Identify the blood parasite species.
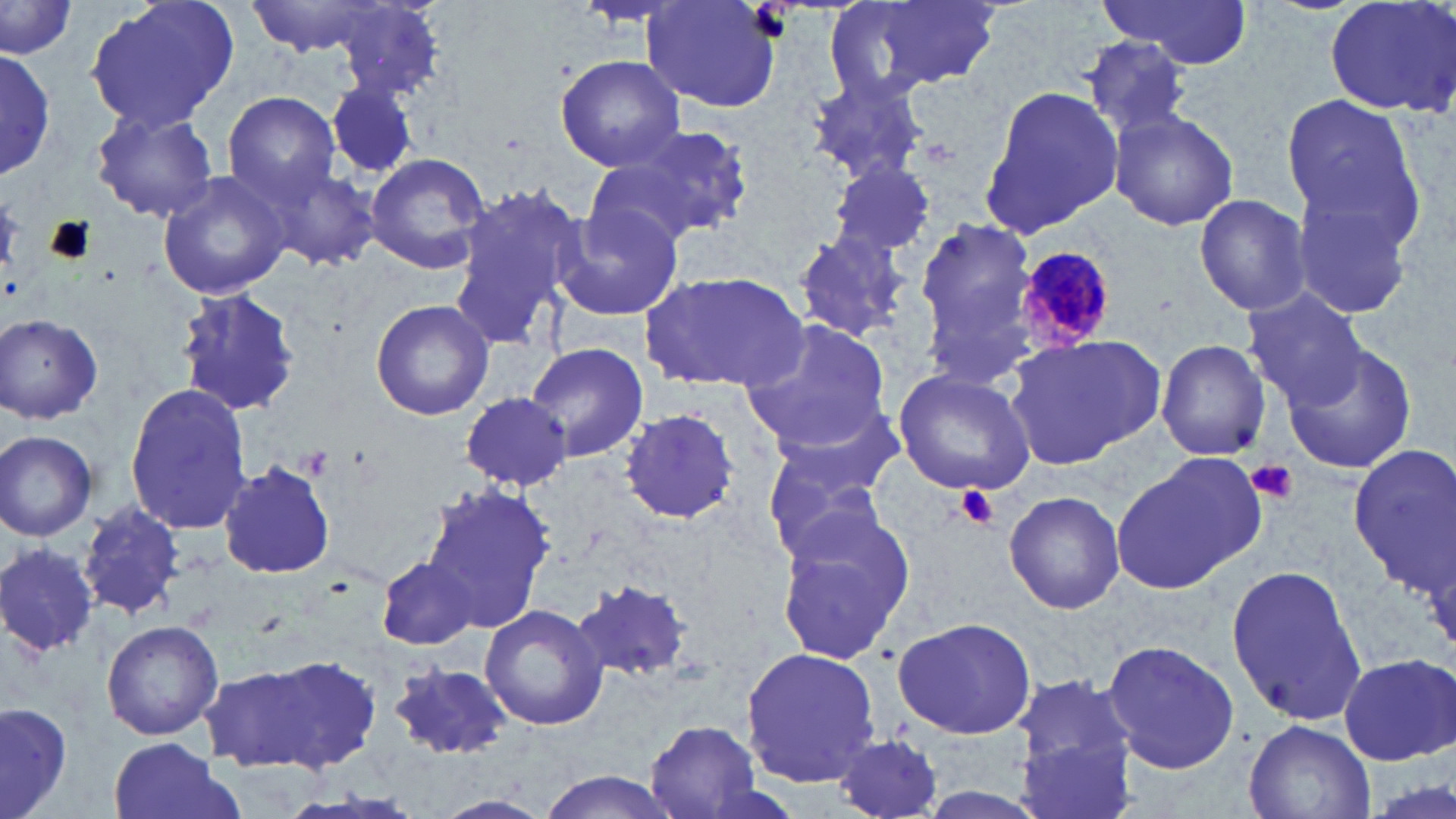
Plasmodium malariae.

Approximate bounding boxes as (x1, y1, x2, y2) in pixels. Plasmodium malariae-infected red blood cell locations: (1011, 243, 1123, 352). Platelet locations: (1247, 460, 1296, 504), (957, 486, 998, 529). Uninfected red blood cell locations: (83, 0, 238, 134), (243, 0, 393, 57), (1099, 0, 1253, 69), (1323, 0, 1456, 118), (643, 1, 783, 115), (824, 1, 991, 102), (0, 2, 76, 61), (330, 2, 446, 98), (1082, 37, 1195, 139), (0, 48, 57, 181), (555, 54, 685, 170), (803, 75, 929, 185), (324, 78, 423, 180), (978, 83, 1125, 239), (223, 90, 340, 203), (1280, 90, 1428, 257), (88, 107, 220, 223), (1109, 108, 1240, 231), (607, 123, 754, 241), (363, 152, 492, 274), (582, 158, 715, 251), (1285, 158, 1429, 324), (256, 161, 380, 270), (829, 161, 940, 260), (157, 171, 291, 301), (446, 180, 584, 352), (1193, 194, 1311, 317), (551, 195, 686, 327), (914, 217, 1038, 364), (792, 231, 916, 342), (638, 269, 810, 393), (173, 287, 301, 420), (1242, 288, 1368, 409), (370, 298, 495, 421), (1, 314, 105, 424), (739, 317, 893, 451), (1001, 335, 1166, 469), (1156, 339, 1271, 460), (525, 341, 650, 461), (1281, 342, 1419, 474), (893, 369, 1035, 496), (124, 383, 253, 535), (460, 390, 573, 491), (769, 404, 909, 500), (621, 409, 739, 525), (0, 430, 98, 541), (1347, 442, 1456, 597), (763, 444, 886, 569), (1111, 454, 1263, 595), (219, 463, 335, 579), (418, 483, 556, 629), (1002, 491, 1126, 613), (79, 502, 184, 620), (776, 504, 918, 661), (0, 541, 100, 659), (377, 556, 478, 650), (1226, 562, 1366, 728), (571, 579, 697, 682), (480, 603, 607, 730), (893, 616, 1036, 741), (101, 619, 224, 741), (1099, 637, 1241, 773), (742, 646, 881, 787), (238, 652, 383, 773), (1337, 653, 1455, 764), (384, 660, 515, 761), (1013, 672, 1139, 777), (0, 700, 71, 819), (1244, 720, 1374, 818), (642, 721, 766, 817), (831, 732, 949, 818), (106, 737, 241, 819), (1017, 740, 1136, 819), (533, 770, 683, 819), (432, 793, 556, 819). Image is 1456×819 pixels. One field of a larger specimen. May-Grünwald-Giemsa stain. Optical microscopy. Captured at 1000x magnification. Thin blood smear.